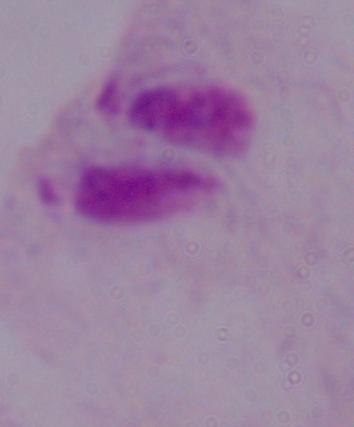

Summary:
  - Modality: photomicrograph
  - Identification: trichomonad
  - Magnification: 1000x